Look for Plasmodium parasites.
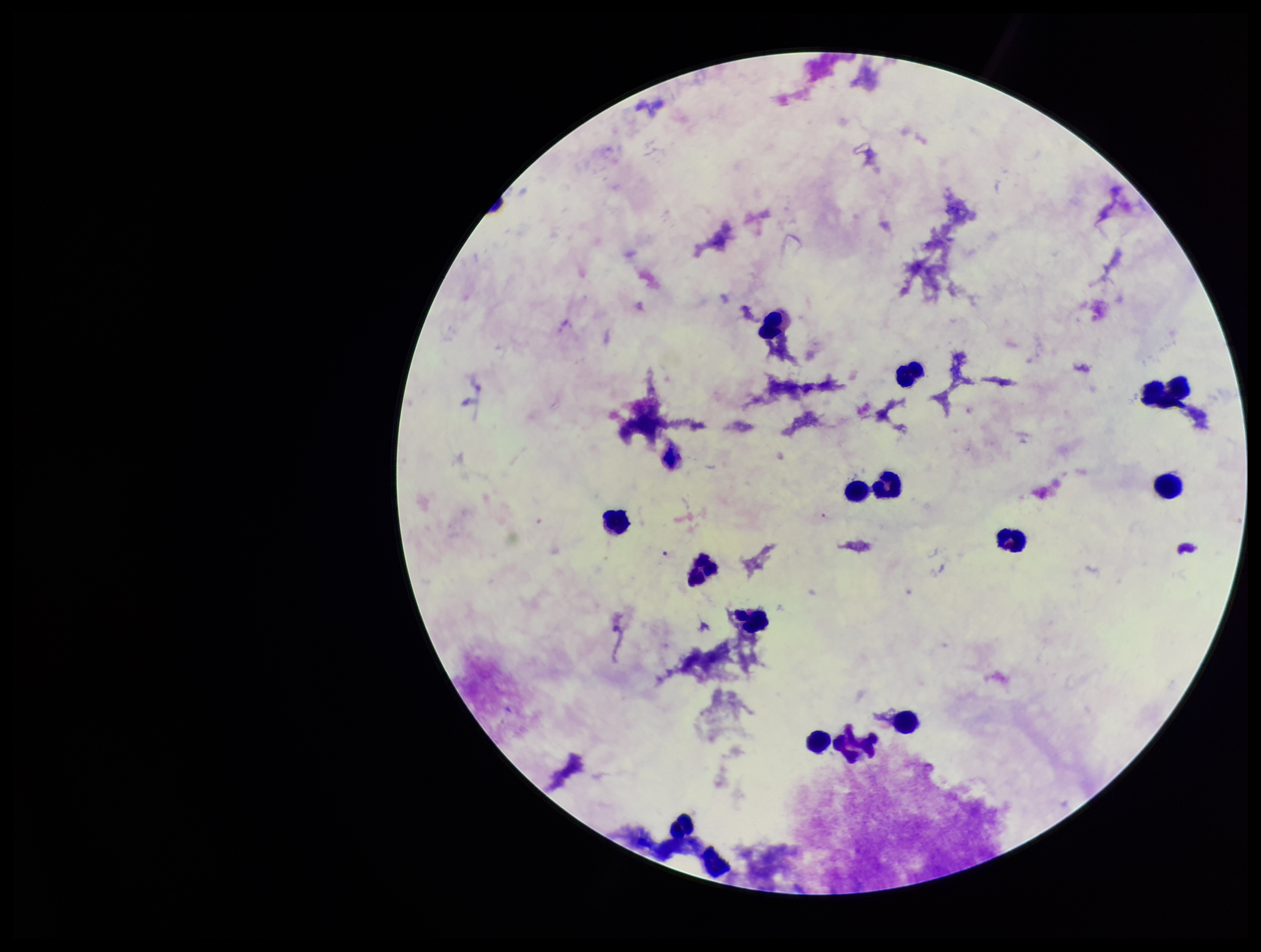
None seen.

leukocyte_count: 14
preparation: thick smear
image_size: 1261×952 pixels
parasite_count: 0
patient_malaria_status: negative
field_of_view: one from this slide
stain: Giemsa
capture: smartphone photograph through the microscope eyepiece